Give the position of every leukocyte.
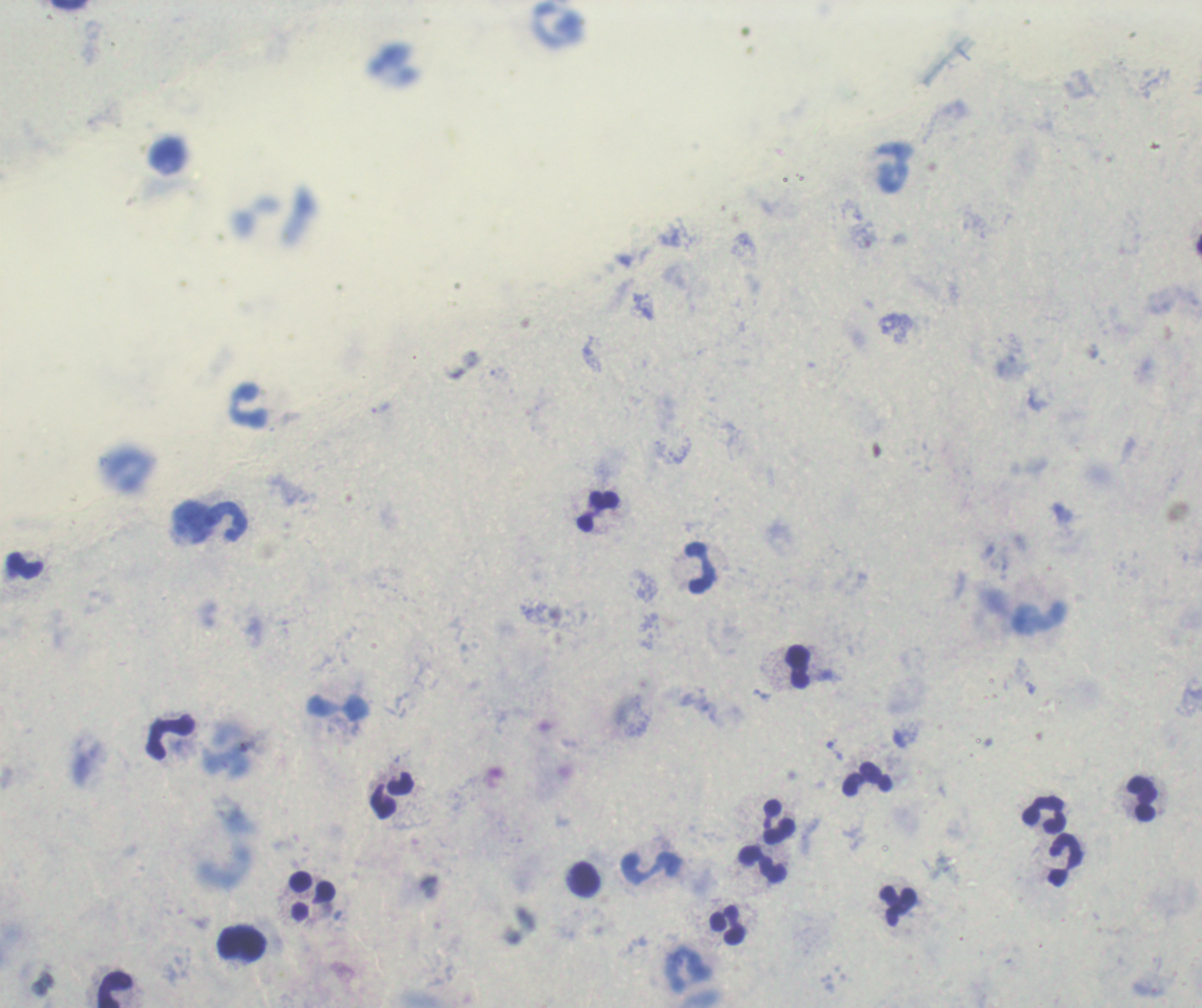
Approximate centers as (x, y) in pixels.
Leukocytes: (250, 406), (598, 511), (191, 521), (227, 521), (699, 569), (1039, 619), (797, 667), (338, 708), (170, 738), (868, 780), (392, 796), (1142, 800), (1045, 815), (780, 822), (1066, 860), (763, 864), (652, 867), (586, 878), (313, 897), (898, 906), (730, 925), (242, 944), (115, 989).

Approximate centers as (x, y) in pixels. Trophozoite locations: (836, 751). Result: positive for malaria parasites. Background quality: unsatisfactory. Image is 1202×1008 pixels. Romanowsky-stained preparation. Thick blood smear. Single field of view. Previously used in a real diagnosis. 100x magnification.